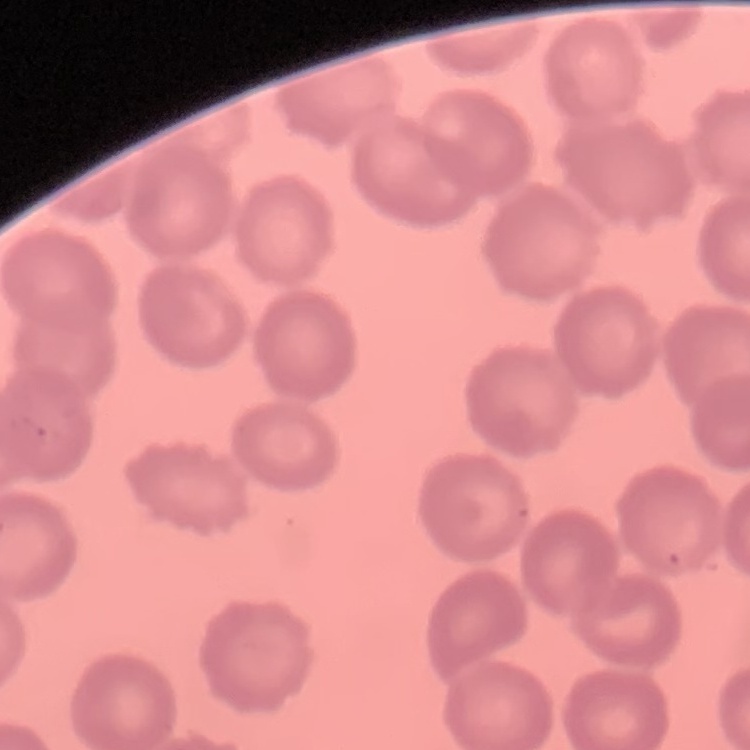
The red blood cells show no rouleaux formation. Field's or Giemsa stain. Square crop of a larger photomicrograph. Thin blood film.